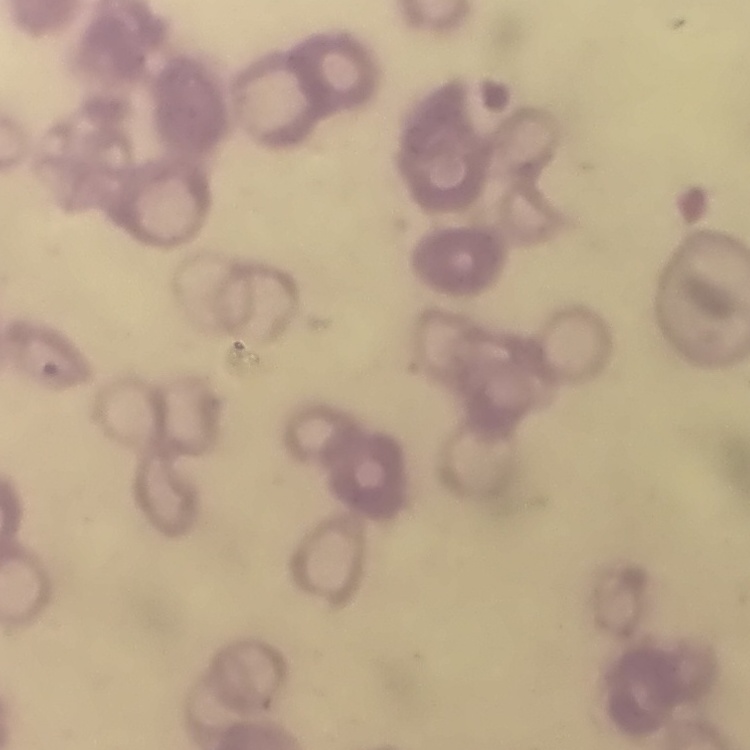

erythrocyte_morphology: rouleaux formation
preparation: thin blood smear
stain: Field's or Giemsa
image_type: square crop of a larger photomicrograph